Classify this cell by malaria status.
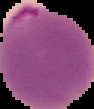

Parasitized.

preparation = thin blood film
image size = 94×109 pixels
image type = segmented cell region on a black background